Locate every malaria parasite and every leukocyte.
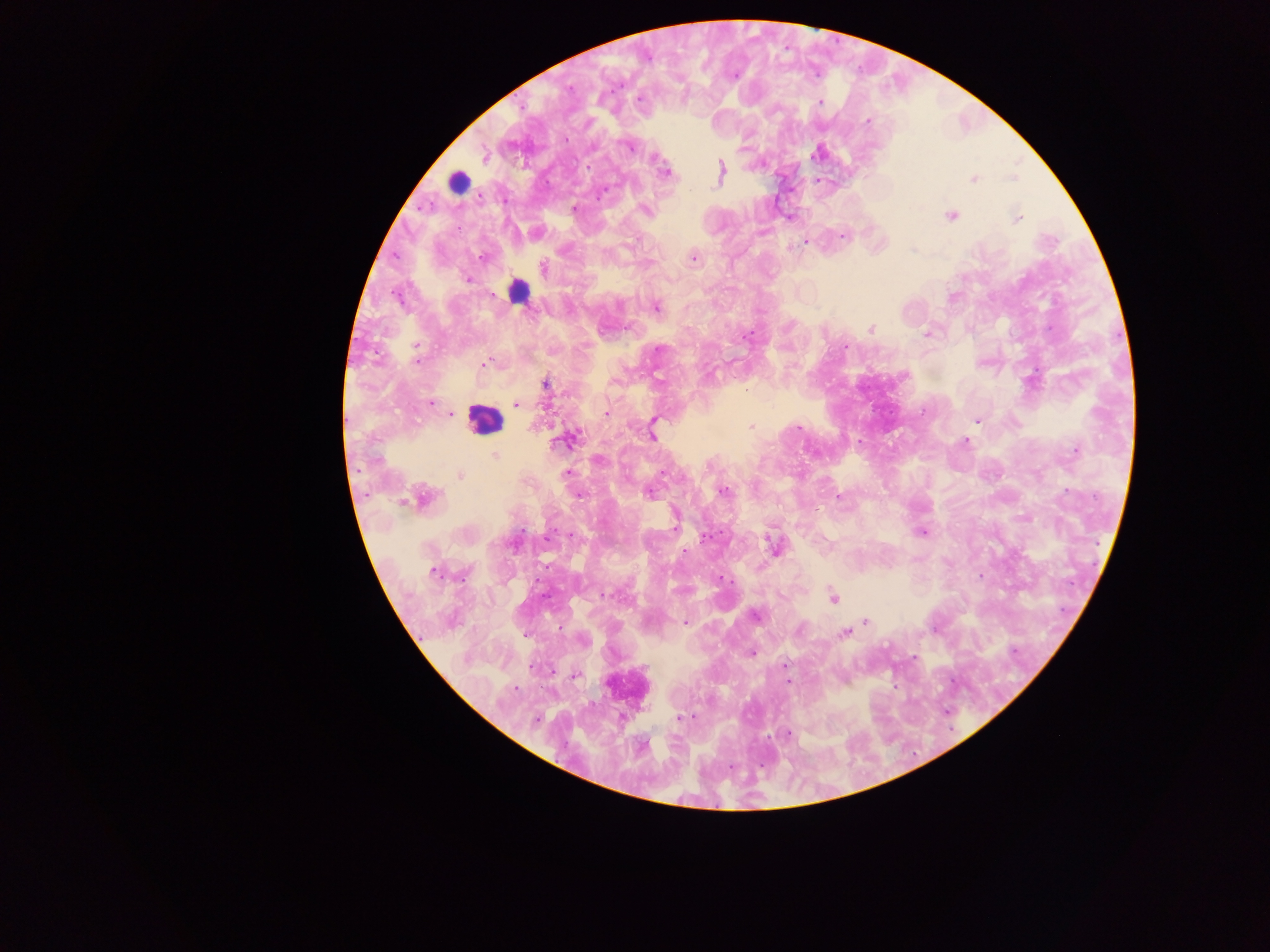

Approximate centers as (x, y) in pixels.
Malaria parasites: (734, 77), (569, 87), (639, 98), (820, 102), (867, 121), (566, 139), (627, 146), (485, 157), (656, 158), (588, 168), (720, 171), (664, 172), (973, 179), (574, 208), (645, 210), (951, 216), (1017, 218), (458, 229), (842, 235), (805, 242), (693, 258), (480, 259), (543, 268), (468, 279), (656, 308), (871, 329), (927, 334), (747, 335), (845, 347), (417, 348), (660, 349), (416, 360), (485, 364), (659, 380), (545, 384), (747, 389), (430, 404), (516, 404), (451, 413), (605, 413), (977, 420), (652, 426), (751, 426), (799, 427), (652, 436), (571, 438), (965, 442), (1075, 450), (495, 455), (598, 460), (566, 473), (460, 476), (723, 491), (649, 493), (578, 495), (838, 497), (424, 499), (675, 523), (922, 532), (547, 538), (703, 538), (774, 545), (686, 551), (433, 572), (980, 576), (720, 577), (606, 595), (833, 597), (755, 616), (865, 620), (685, 623), (799, 631), (844, 633), (751, 653), (785, 666), (532, 667), (575, 675), (788, 681), (514, 689), (680, 717), (536, 719), (789, 733).
Leukocytes: (458, 183), (484, 418), (628, 685).
One object is labeled both malaria parasite and leukocyte by the source: (518, 291).

Summary:
  - Preparation: thick blood smear
  - Field of view: single
  - Country: Ghana
  - Capture: mobile-phone photograph through a microscope
  - Image size: 1270×952 pixels